Classify this cell by malaria status.
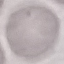

It is uninfected.

{
  "preparation": "thin blood film",
  "stain": "Giemsa",
  "image_type": "automatically extracted cell patch, resized to 64 × 64 pixels",
  "capture": "smartphone through the microscope eyepiece"
}